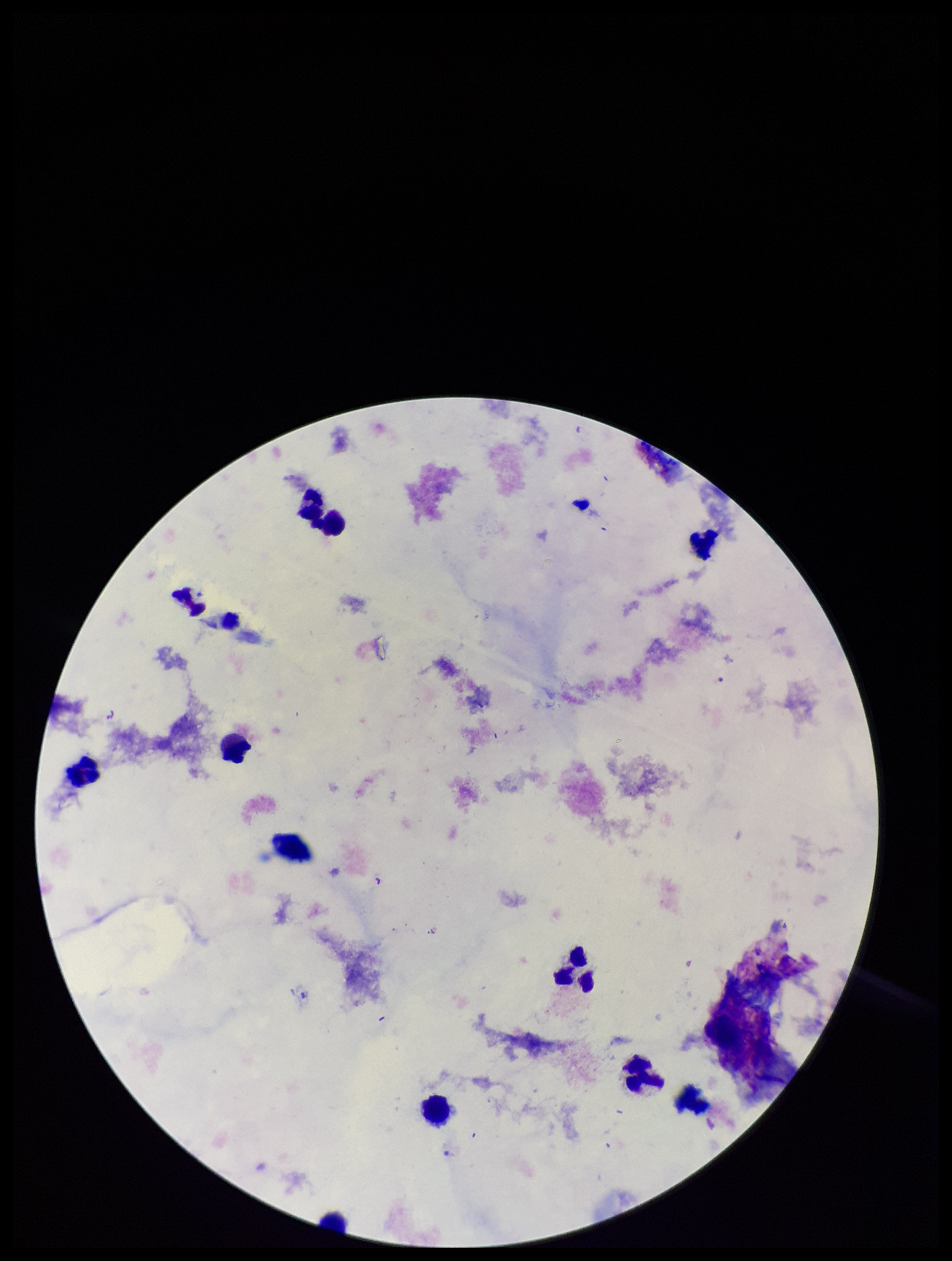
Parasite count: 0. Image is 952×1261 pixels. Stained with Giemsa. Patient malaria status: negative. Smartphone photograph taken through the eyepiece of a microscope. One field from this slide. Plasmodium parasites: none seen. Leukocyte count: 11. Preparation: thick blood smear.